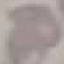
malaria_status: uninfected
preparation: thin blood film
stain: Giemsa
capture: smartphone through the microscope eyepiece
image_type: automatically extracted cell patch, resized to 64 × 64 pixels